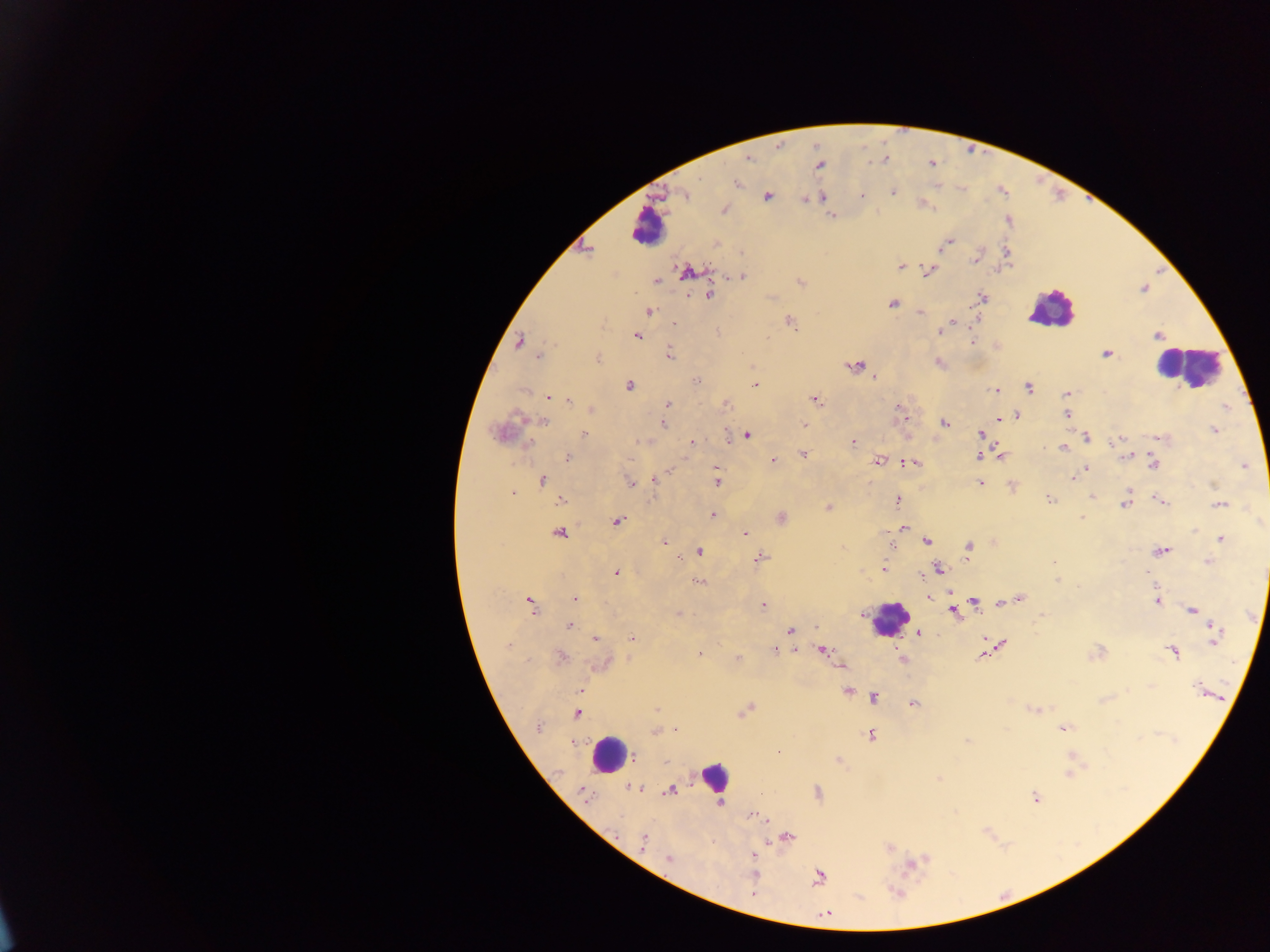

field_of_view: single
country: Ghana
image_size: 1270×952 pixels
malaria_parasite_locations: 'approximate centers as [x, y] in pixels: [749, 158], [819, 165], [737, 184], [892, 192], [685, 194], [861, 195], [767, 196], [822, 197], [805, 200], [724, 209], [832, 216], [947, 243], [1007, 252], [742, 253], [975, 259], [901, 267], [929, 270], [687, 272], [741, 277], [655, 281], [800, 283], [709, 295], [982, 297], [892, 303], [650, 311], [920, 312], [955, 322], [674, 323], [792, 324], [718, 332], [940, 332], [1158, 335], [637, 336], [519, 342], [972, 342], [670, 354], [1106, 354], [540, 356], [597, 359], [940, 363], [856, 366], [874, 377], [696, 381], [629, 385], [755, 385], [1029, 387], [996, 389], [523, 391], [1066, 394], [549, 396], [815, 399], [568, 400], [668, 403], [724, 405], [898, 407], [590, 410], [1066, 414], [1017, 416], [905, 419], [997, 419], [544, 421], [945, 422], [662, 424], [804, 425], [1214, 431], [500, 432], [584, 433], [979, 434], [728, 436], [747, 436], [1087, 437], [1160, 438], [1115, 441], [691, 442], [853, 442], [1063, 448], [804, 454], [1128, 455], [1000, 456], [567, 457], [979, 457], [773, 461], [878, 461], [913, 463], [1154, 465], [1244, 466], [716, 468], [1086, 469], [655, 478], [1073, 478], [542, 481], [629, 482], [716, 482], [980, 483], [1213, 486], [512, 492], [1092, 497], [898, 500], [1050, 500], [1160, 500], [561, 501], [1220, 504], [1125, 505], [828, 507], [713, 514], [781, 517], [1082, 517], [616, 521], [903, 528], [559, 533], [746, 533], [1220, 538], [927, 541], [664, 542], [1216, 544], [892, 546], [968, 548], [698, 551], [1161, 551], [759, 558], [1208, 561], [1054, 562], [883, 569], [940, 569], [616, 573], [1146, 574], [922, 578], [697, 581], [1057, 581], [929, 596], [575, 599], [1020, 599], [1156, 601], [973, 602], [531, 603], [764, 605], [1192, 610], [954, 612], [678, 614], [569, 626], [790, 631], [919, 633], [1214, 636], [632, 638], [595, 639], [1000, 644], [508, 646], [823, 650], [775, 651], [1173, 652], [699, 654], [1095, 654], [560, 656], [982, 656], [902, 658], [737, 659], [602, 663], [580, 689], [1200, 690], [847, 691], [874, 698], [914, 703], [657, 709], [745, 710], [1035, 710], [577, 713], [538, 727], [1062, 728], [676, 730], [654, 732], [871, 736], [967, 740], [634, 757], [1073, 758], [838, 761], [667, 762], [1069, 773], [939, 779], [635, 788], [670, 790], [818, 792], [585, 796], [1035, 797], [720, 802], [752, 816], [788, 837], [643, 841], [890, 848], [754, 855], [668, 858], [914, 864], [754, 872], [819, 877], [896, 893], [825, 913]'
preparation: thick blood smear
capture: mobile-phone photograph through a microscope
leukocyte_locations: 'approximate centers as [x, y] in pixels: [647, 227], [1051, 308], [1186, 367], [890, 619], [608, 754], [714, 775]'